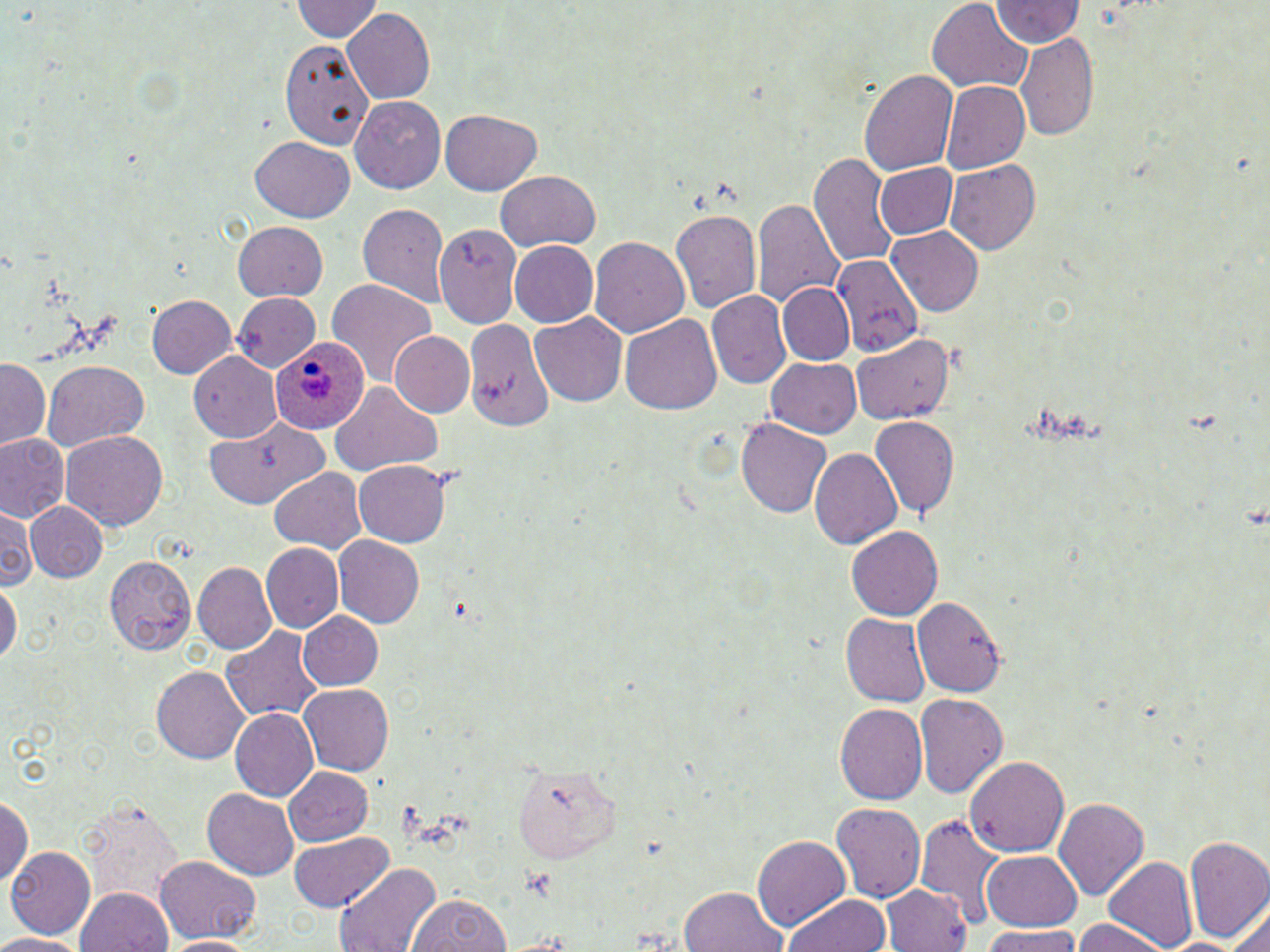
Summary:
  - Coordinate format: approximate bounding boxes as (x1,y1)-(x2,y2) corner pairs in pixels
  - Platelet locations: (524,866)-(554,899)
  - Plasmodium ovale-infected red blood cell locations: (271,332)-(370,432)
  - Uninfected red blood cell locations: (292,0)-(383,43), (926,0)-(1031,92), (990,1)-(1084,49), (343,9)-(434,103), (1014,30)-(1099,144), (280,36)-(372,150), (860,68)-(959,176), (942,82)-(1030,172), (351,95)-(446,192), (440,109)-(544,195), (250,135)-(354,222), (810,153)-(896,269), (944,157)-(1042,254), (872,162)-(959,242), (494,170)-(601,252), (358,200)-(451,304), (751,200)-(844,311), (670,208)-(762,314), (232,222)-(326,300), (434,224)-(521,328), (886,225)-(988,315), (589,235)-(689,335), (510,242)-(598,329), (830,255)-(926,359), (326,278)-(439,387), (777,282)-(856,366), (709,289)-(790,389), (228,291)-(327,369), (146,295)-(237,380), (530,311)-(627,408), (619,312)-(723,413), (461,313)-(556,434), (391,331)-(474,416), (852,338)-(966,424), (189,353)-(279,438), (767,358)-(861,438), (1,359)-(52,450), (41,361)-(149,451), (330,384)-(443,473), (867,417)-(958,522), (737,418)-(830,517), (204,419)-(326,508), (63,430)-(168,531), (1,432)-(69,524), (808,446)-(904,550), (353,461)-(454,546), (266,466)-(369,554), (26,501)-(108,582), (0,509)-(37,590), (847,526)-(943,622), (332,536)-(425,628), (261,544)-(342,632), (104,554)-(196,651), (192,562)-(276,655), (0,578)-(20,671), (913,595)-(1006,698), (296,610)-(384,692), (840,614)-(930,707), (221,626)-(323,725), (151,664)-(248,764), (297,683)-(393,775), (914,694)-(1008,798), (835,704)-(927,808), (230,710)-(319,802), (966,756)-(1069,858), (515,761)-(619,864), (282,767)-(372,848), (202,789)-(298,878), (76,793)-(184,909), (0,795)-(33,886), (1055,798)-(1149,907), (832,801)-(926,903), (916,811)-(1004,922), (289,834)-(393,912), (752,834)-(850,935), (1183,837)-(1269,942), (7,847)-(98,940), (981,850)-(1082,932), (1103,855)-(1198,951), (155,857)-(261,943), (335,863)-(441,952), (884,883)-(973,952), (75,885)-(173,952), (676,886)-(787,952), (782,891)-(888,952), (406,892)-(509,952), (1229,900)-(1270,952), (1072,920)-(1166,952), (984,929)-(1088,952), (0,932)-(92,951), (164,935)-(256,951)
  - Slide-level diagnosis: Plasmodium ovale
  - Field of view: single
  - Stain: May-Grünwald-Giemsa
  - Preparation: thin blood smear
  - Magnification: 1000x
  - Modality: light microscopy
  - Image size: 1270×952 pixels